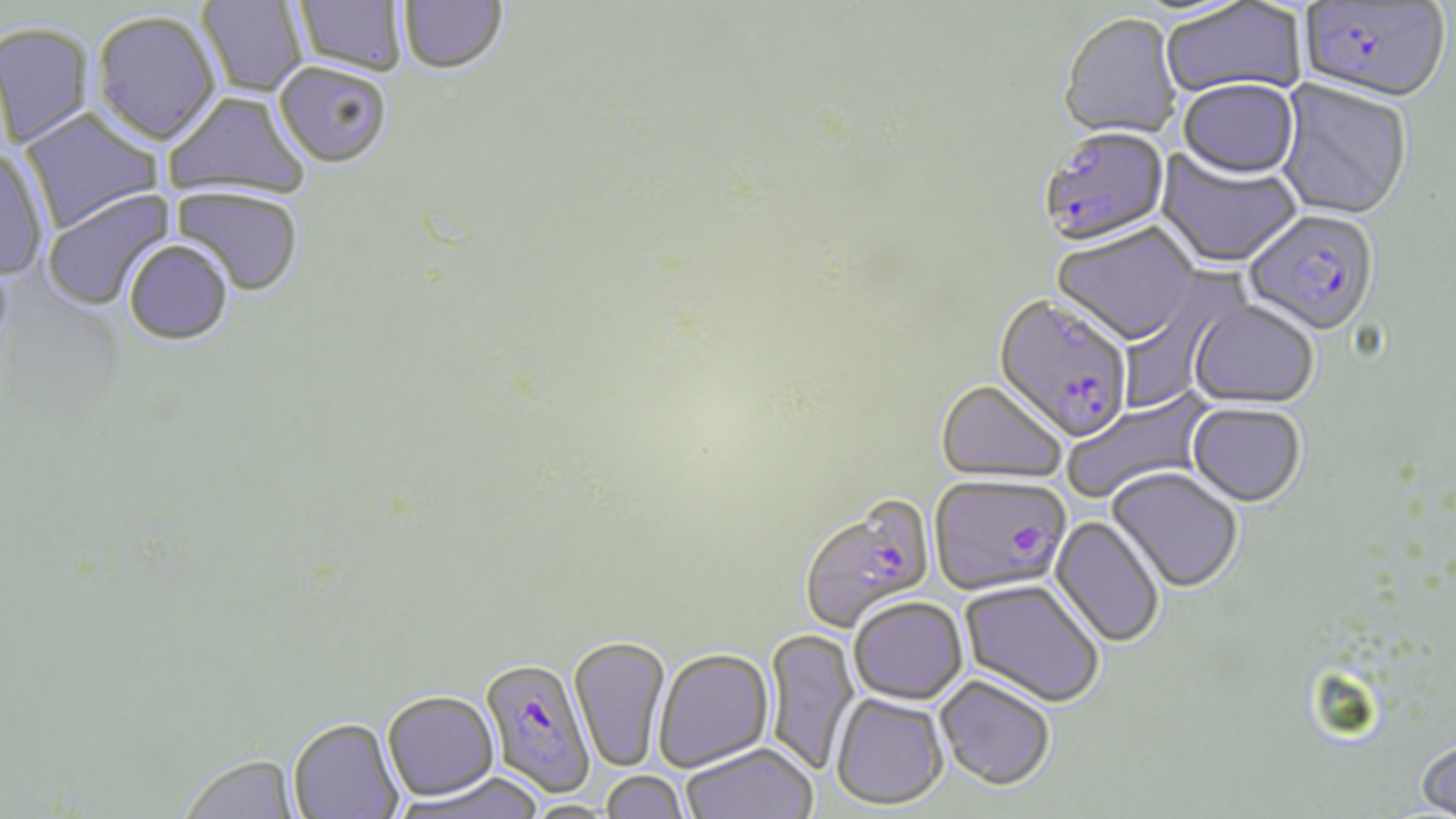
slide-level diagnosis = Plasmodium falciparum
image size = 1456×819 pixels
preparation = thin blood smear
uninfected red blood cell locations = approximate bounding boxes as (x1,y1)-(x2,y2) corner pairs in pixels: (197,0)-(308,98), (294,0)-(406,76), (399,0)-(507,74), (1160,1)-(1307,102), (92,10)-(221,146), (1059,15)-(1182,143), (0,22)-(95,148), (274,61)-(393,168), (1177,81)-(1300,183), (1274,81)-(1412,223), (162,90)-(310,202), (19,108)-(164,233), (0,148)-(50,280), (1155,150)-(1302,270), (170,186)-(304,297), (43,188)-(176,311), (1051,225)-(1199,349), (124,239)-(233,347), (1117,270)-(1248,412), (1188,301)-(1319,410), (935,381)-(1068,487), (1062,390)-(1217,504), (1187,403)-(1306,508), (1107,467)-(1242,593), (1049,515)-(1165,649), (960,579)-(1106,707), (849,596)-(968,704), (765,628)-(860,776), (570,636)-(671,774), (653,648)-(774,772), (935,674)-(1056,790), (382,691)-(499,803), (830,692)-(948,809), (288,719)-(404,819), (1415,737)-(1456,818), (682,742)-(818,819), (181,755)-(299,819), (600,770)-(690,819), (398,774)-(545,819), (522,800)-(620,818)
field of view = single
magnification = 1000x
modality = optical microscopy
Plasmodium falciparum-infected red blood cell locations = approximate bounding boxes as (x1,y1)-(x2,y2) corner pairs in pixels: (1299,1)-(1450,107), (1039,128)-(1170,250), (1243,210)-(1379,340), (992,295)-(1132,445), (927,476)-(1071,596), (799,496)-(936,634), (478,658)-(597,798)
stain = May-Grünwald-Giemsa